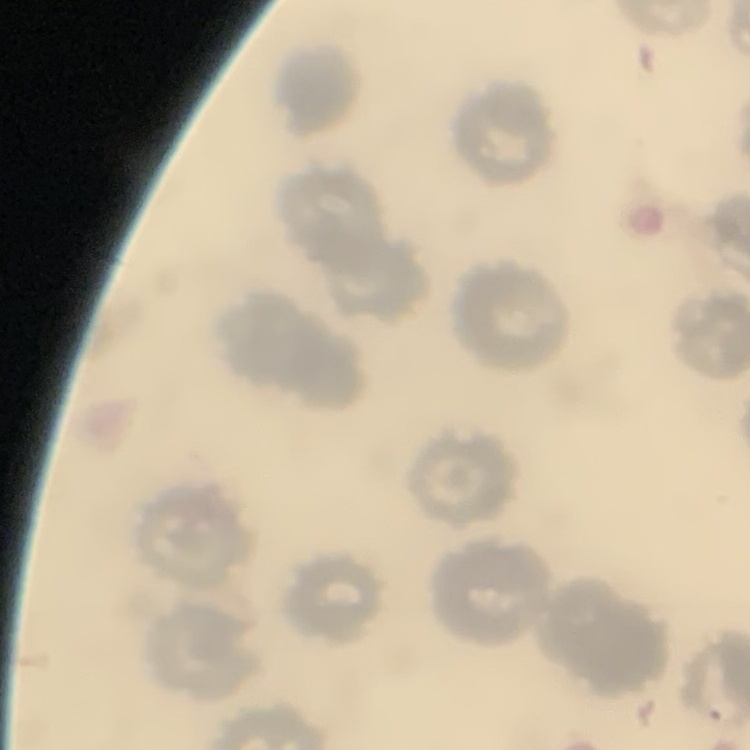
The red blood cells exhibit no rouleaux formation. Stained with either Field's or Giemsa. Thin peripheral smear. Square crop of a larger photomicrograph.